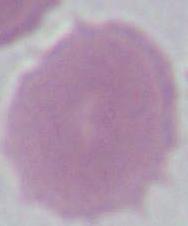
Summary:
  - Magnification: 1000x
  - Identification: red blood cell
  - Modality: micrograph